Describe the morphology of the red blood cells.
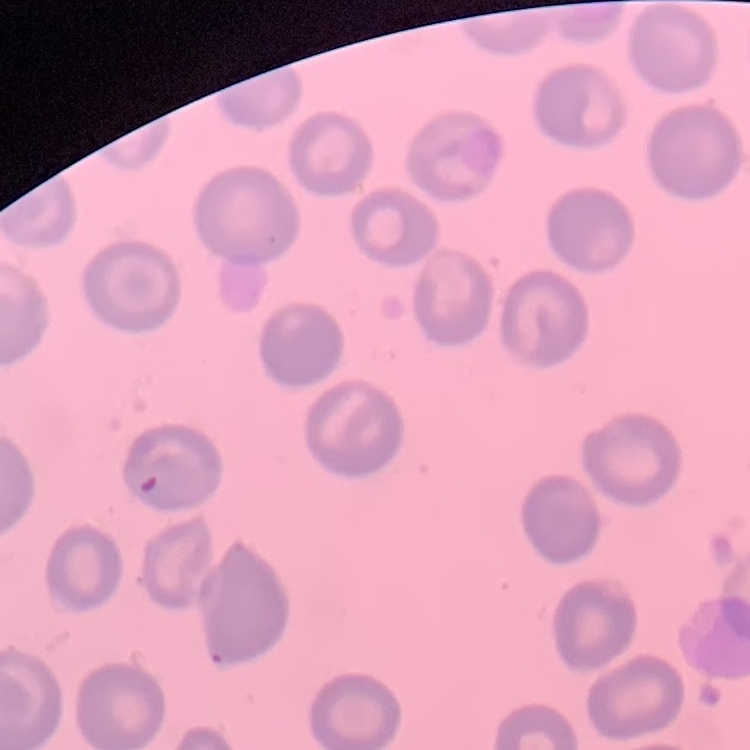
They show no rouleaux formation.

Square crop of a larger photomicrograph. Stained with either Field's or Giemsa. Thin peripheral smear.